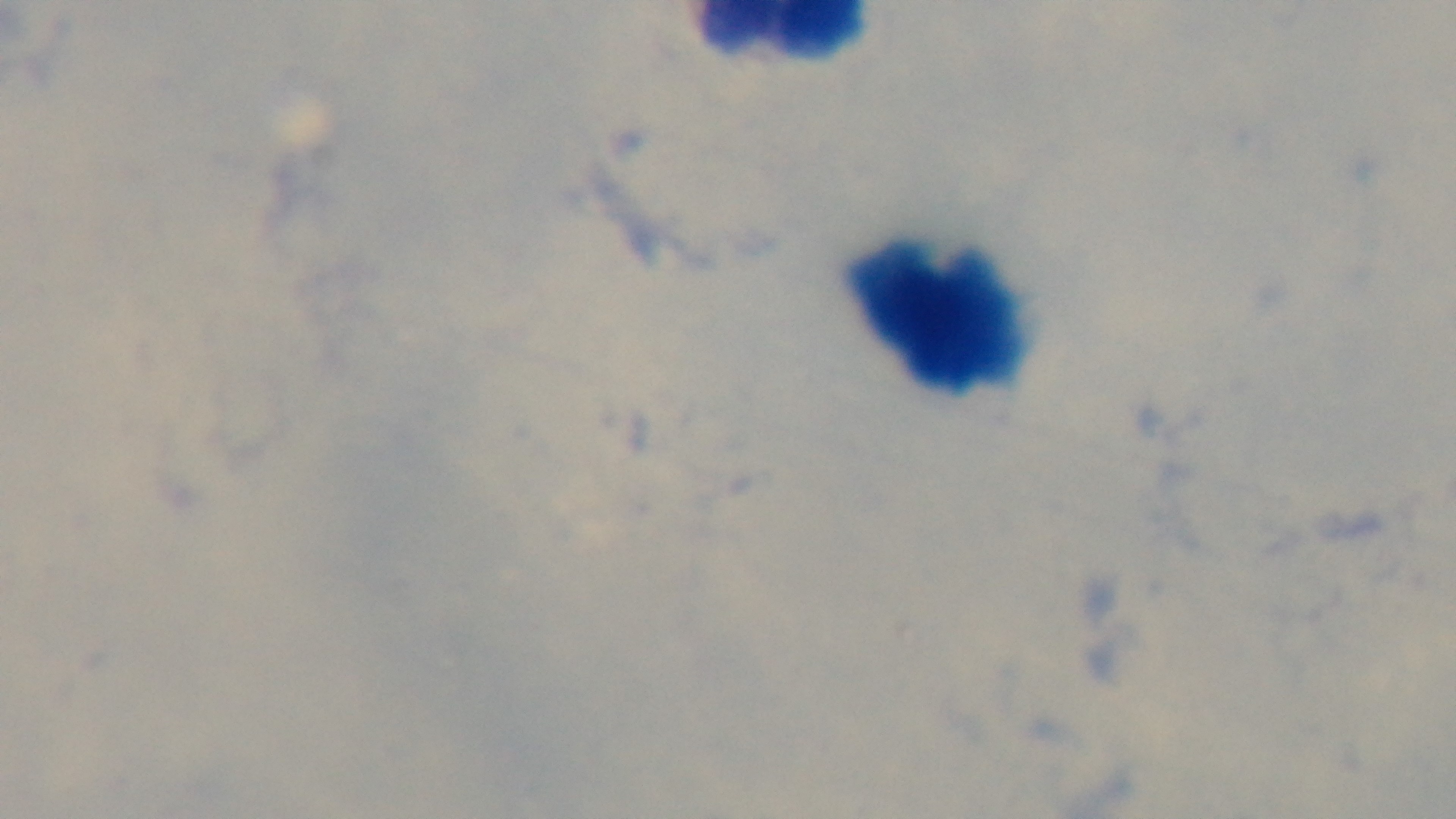
{
  "malaria_status": "uninfected",
  "stain": "Giemsa",
  "field_of_view": "one from the slide",
  "preparation": "thick",
  "capture": "mounted 4K digital camera",
  "objective": "100x oil immersion",
  "modality": "light microscopy"
}